State which cell type is depicted.
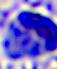

This is a leukocyte.

400x magnification. Micrograph.